Describe the morphology of the erythrocytes.
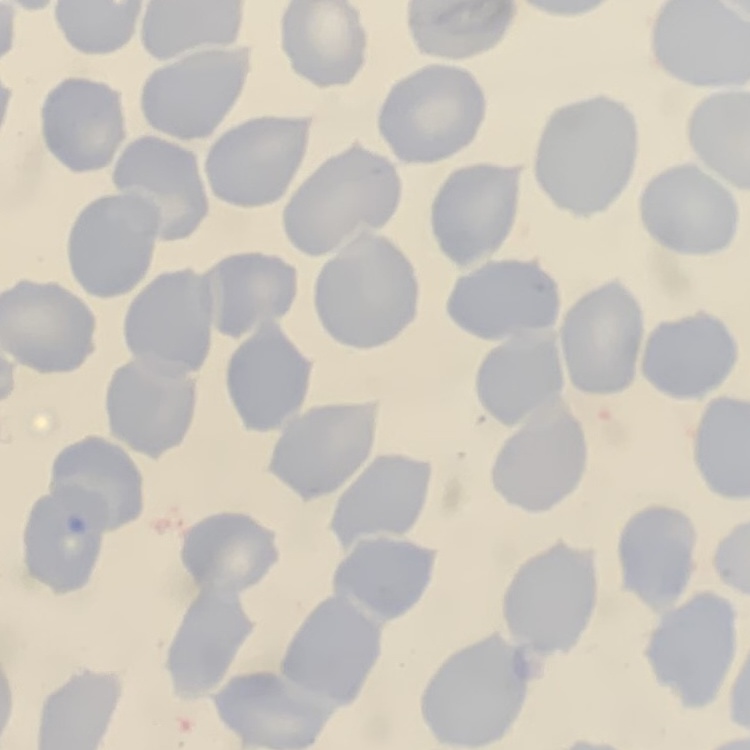
They show no rouleaux formation.

Square crop of a larger photomicrograph. Thin blood smear. Stained with either Field's or Giemsa.